Assess the morphology of the red blood cells.
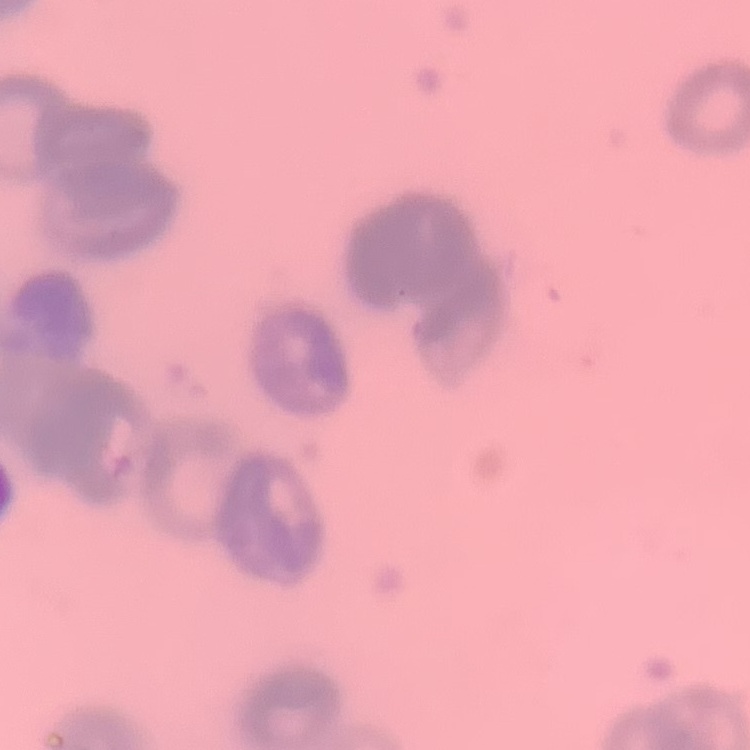

They show rouleaux formation.

Square crop of a larger photomicrograph. Thin blood film. Stained with either Field's or Giemsa.